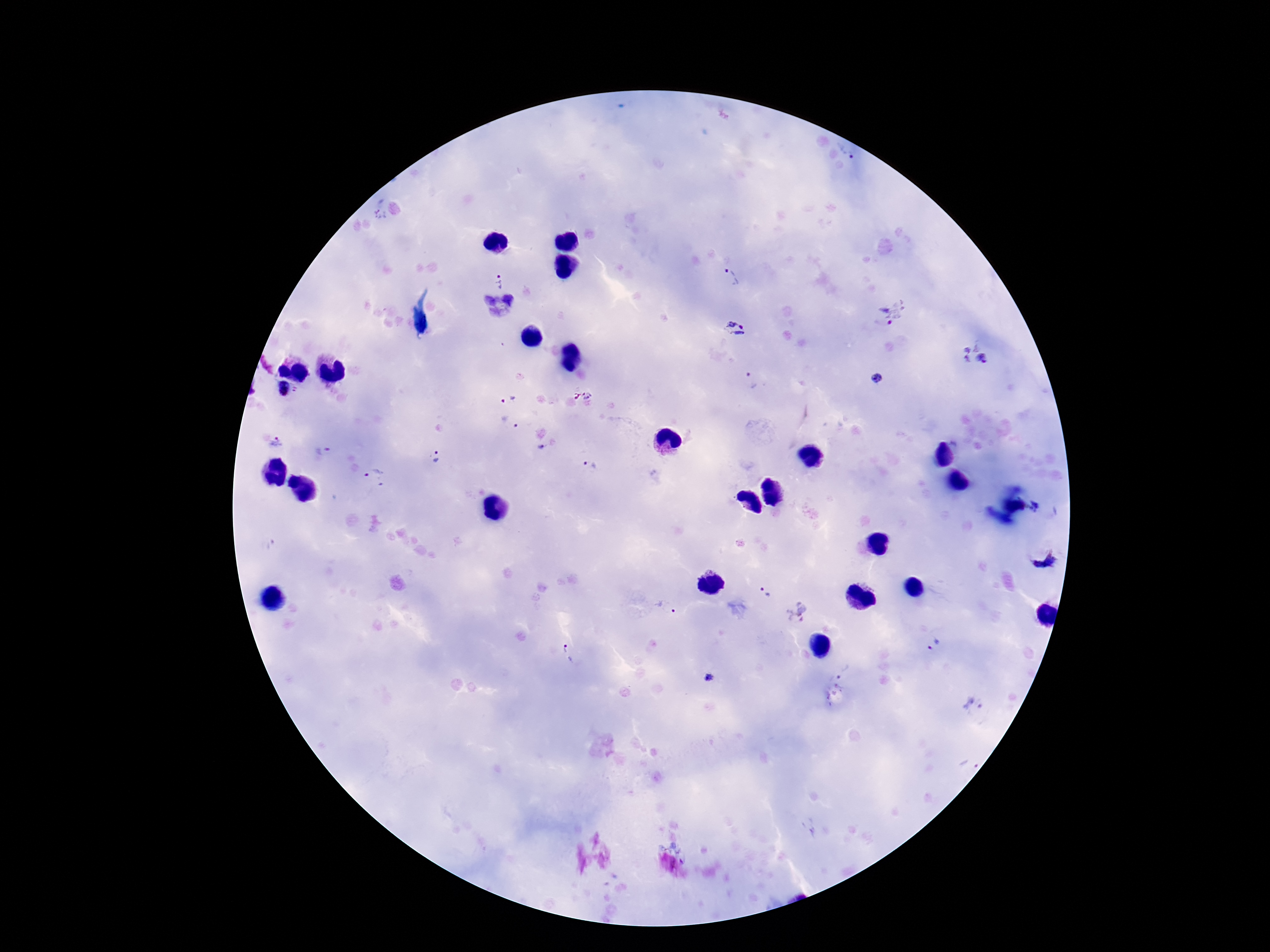
image size = 1270×952 pixels
Plasmodium parasite locations = approximate centers as [x, y] in pixels: [845, 153], [731, 278], [499, 281], [498, 308], [892, 312], [736, 330], [975, 355], [750, 380], [880, 381], [584, 397], [506, 400], [510, 423], [277, 442], [539, 449], [324, 450], [436, 456], [591, 464], [373, 477], [1037, 509], [267, 545], [1043, 558], [765, 592], [667, 607], [796, 612], [934, 645], [567, 656], [709, 677], [972, 704], [969, 764]
patient malaria status = positive
magnification = 100x
stain = Giemsa
capture = smartphone camera through the microscope eyepiece
preparation = thick blood smear
field of view = single